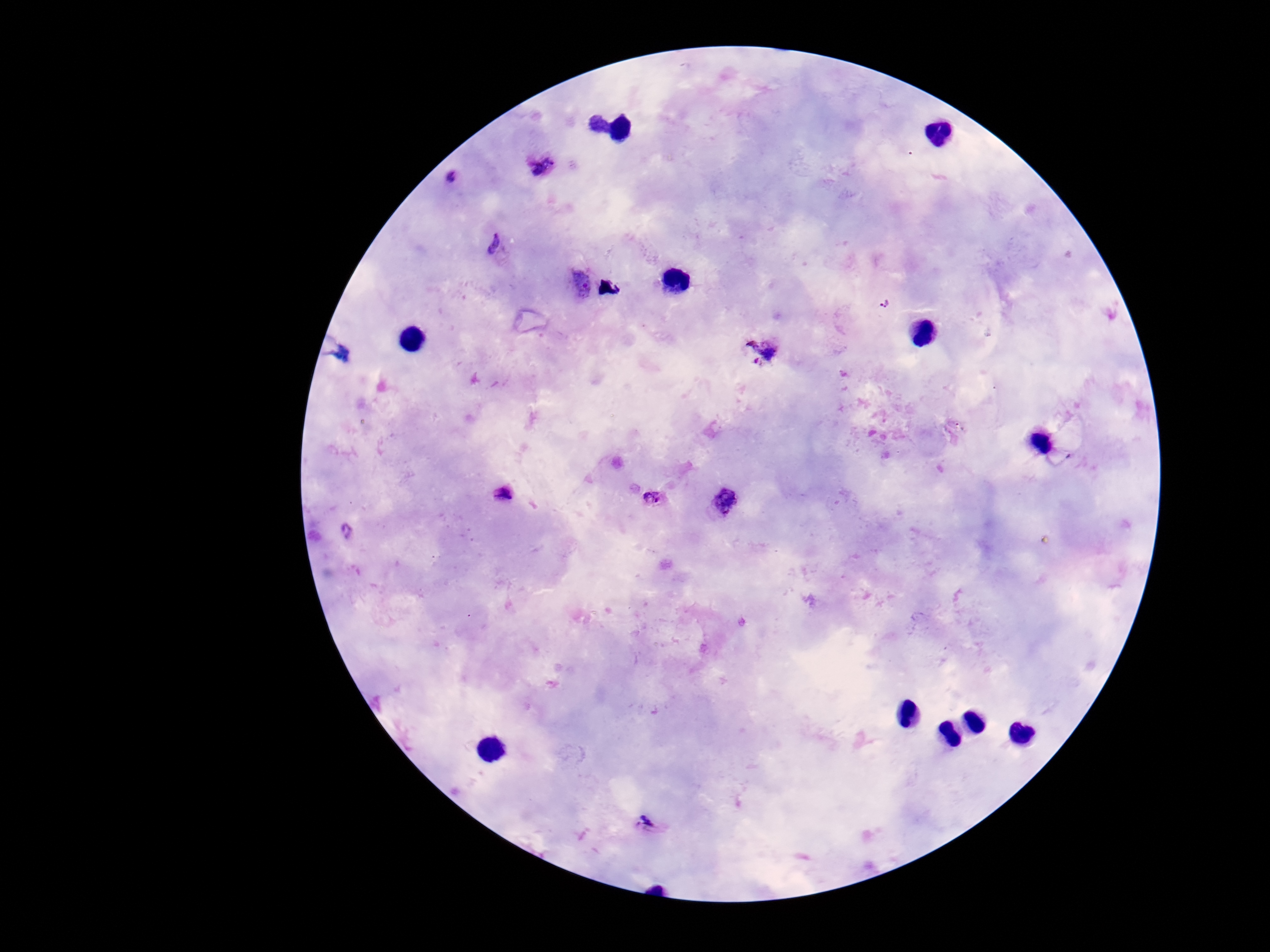
image_size: 1270×952 pixels
field_of_view: one from this slide
patient_malaria_status: positive
stain: Giemsa
preparation: thick blood smear
magnification: 100x
plasmodium_parasite_locations: 'approximate centers as [x, y] in pixels: [542, 166], [454, 179], [494, 242], [581, 283], [885, 304], [761, 350], [505, 494], [654, 497], [724, 501], [346, 531], [649, 822]'
capture: smartphone camera through the microscope eyepiece